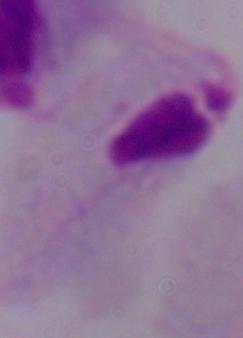
Micrograph. A trichomonad is shown. Captured at 1000x magnification.